Locate platelets.
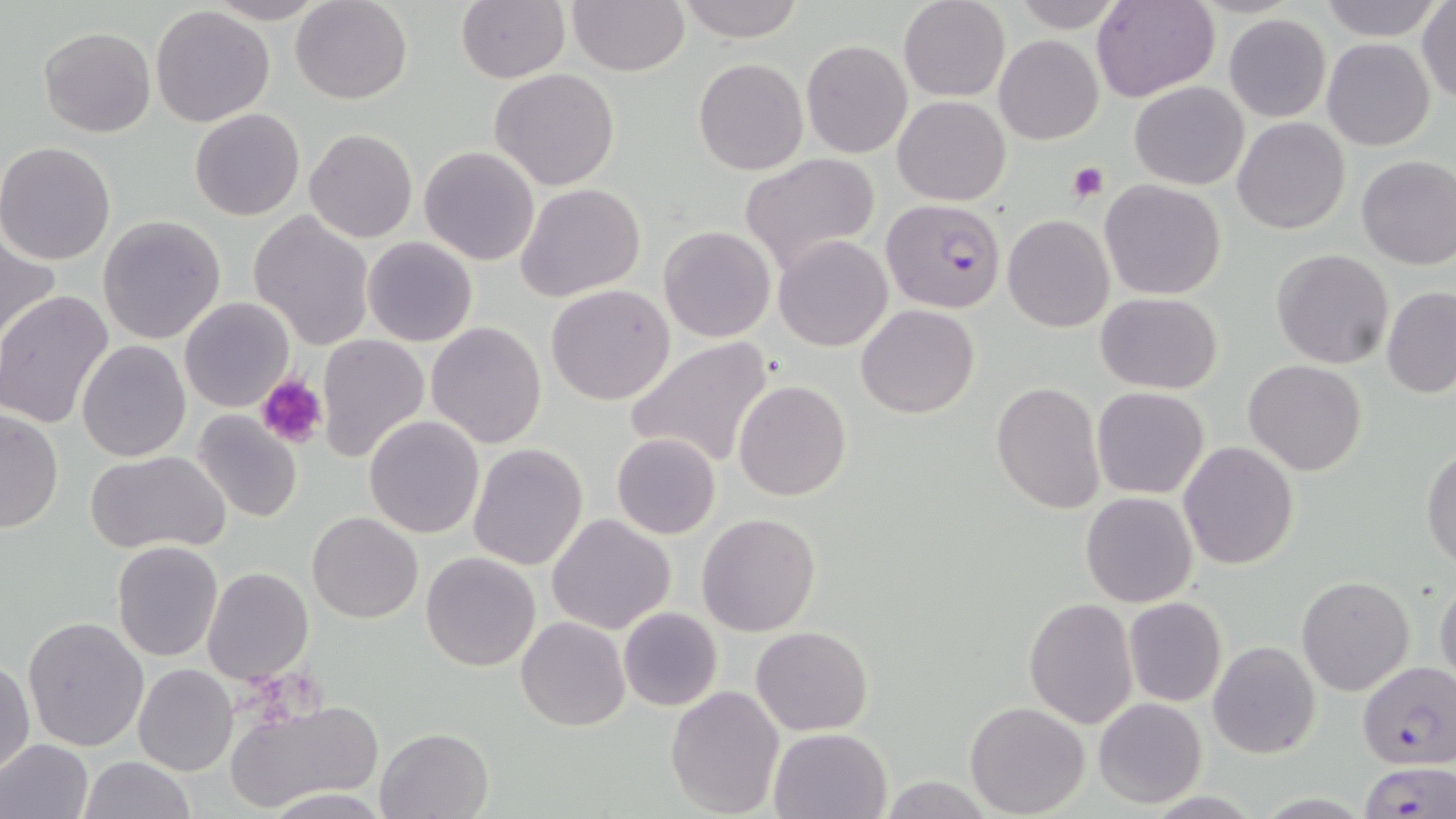

Approximate bounding boxes as (x1, y1, x2, y2) in pixels.
Platelets: (1066, 162, 1108, 203), (256, 375, 328, 449).

slide-level diagnosis = Plasmodium falciparum
preparation = thin blood smear
magnification = 1000x
modality = light microscopy
field of view = one of a larger specimen
uninfected red blood cell locations = approximate bounding boxes as (x1, y1, x2, y2) in pixels: (203, 0, 332, 24), (291, 0, 412, 104), (456, 0, 570, 84), (567, 0, 689, 76), (675, 0, 804, 43), (898, 0, 1011, 101), (1004, 0, 1130, 33), (1320, 0, 1439, 38), (1416, 0, 1456, 106), (1090, 1, 1219, 101), (150, 7, 277, 127), (1223, 14, 1331, 122), (39, 26, 156, 137), (994, 35, 1103, 144), (1321, 38, 1435, 151), (801, 39, 912, 159), (693, 57, 808, 176), (488, 69, 620, 191), (1129, 81, 1249, 189), (893, 96, 1010, 204), (190, 108, 305, 221), (1232, 117, 1350, 235), (303, 129, 417, 244), (0, 141, 119, 265), (419, 146, 540, 265), (739, 153, 879, 278), (1355, 155, 1456, 270), (1098, 180, 1226, 300), (515, 183, 645, 302), (248, 210, 375, 351), (1003, 214, 1113, 332), (97, 215, 226, 344), (658, 225, 777, 343), (1, 230, 60, 349), (773, 235, 892, 352), (362, 236, 478, 347), (1271, 248, 1395, 369), (546, 284, 677, 405), (1382, 285, 1456, 398), (0, 291, 116, 432), (1095, 292, 1224, 394), (179, 297, 295, 412), (856, 304, 980, 418), (426, 321, 546, 448), (317, 334, 432, 462), (626, 337, 776, 470), (76, 339, 190, 461), (1244, 360, 1366, 476), (734, 380, 851, 502), (990, 382, 1105, 515), (1092, 387, 1209, 498), (0, 408, 64, 536), (191, 410, 305, 527), (364, 415, 485, 538), (611, 433, 722, 540), (1179, 441, 1298, 571), (467, 443, 589, 571), (1422, 445, 1456, 569), (86, 450, 230, 555), (1080, 492, 1199, 608), (307, 513, 422, 623), (696, 513, 821, 636), (546, 514, 676, 636), (111, 540, 224, 661), (421, 552, 541, 673), (203, 567, 314, 684), (1296, 575, 1413, 695), (1434, 575, 1456, 684), (1024, 597, 1139, 729), (1124, 598, 1227, 706), (617, 608, 722, 711), (516, 616, 630, 730), (22, 617, 149, 753), (750, 626, 873, 735), (1208, 639, 1322, 758), (0, 657, 34, 777), (133, 664, 238, 775), (666, 685, 785, 817), (225, 697, 380, 810), (1093, 697, 1206, 808), (964, 702, 1090, 818), (769, 727, 892, 818), (375, 728, 493, 818), (0, 738, 94, 819), (79, 756, 195, 818), (878, 777, 996, 817), (260, 787, 391, 818)
Plasmodium falciparum-infected red blood cell locations = approximate bounding boxes as (x1, y1, x2, y2) in pixels: (880, 197, 1006, 314), (1357, 661, 1456, 767), (1356, 760, 1456, 818)
stain = May-Grünwald-Giemsa
image size = 1456×819 pixels